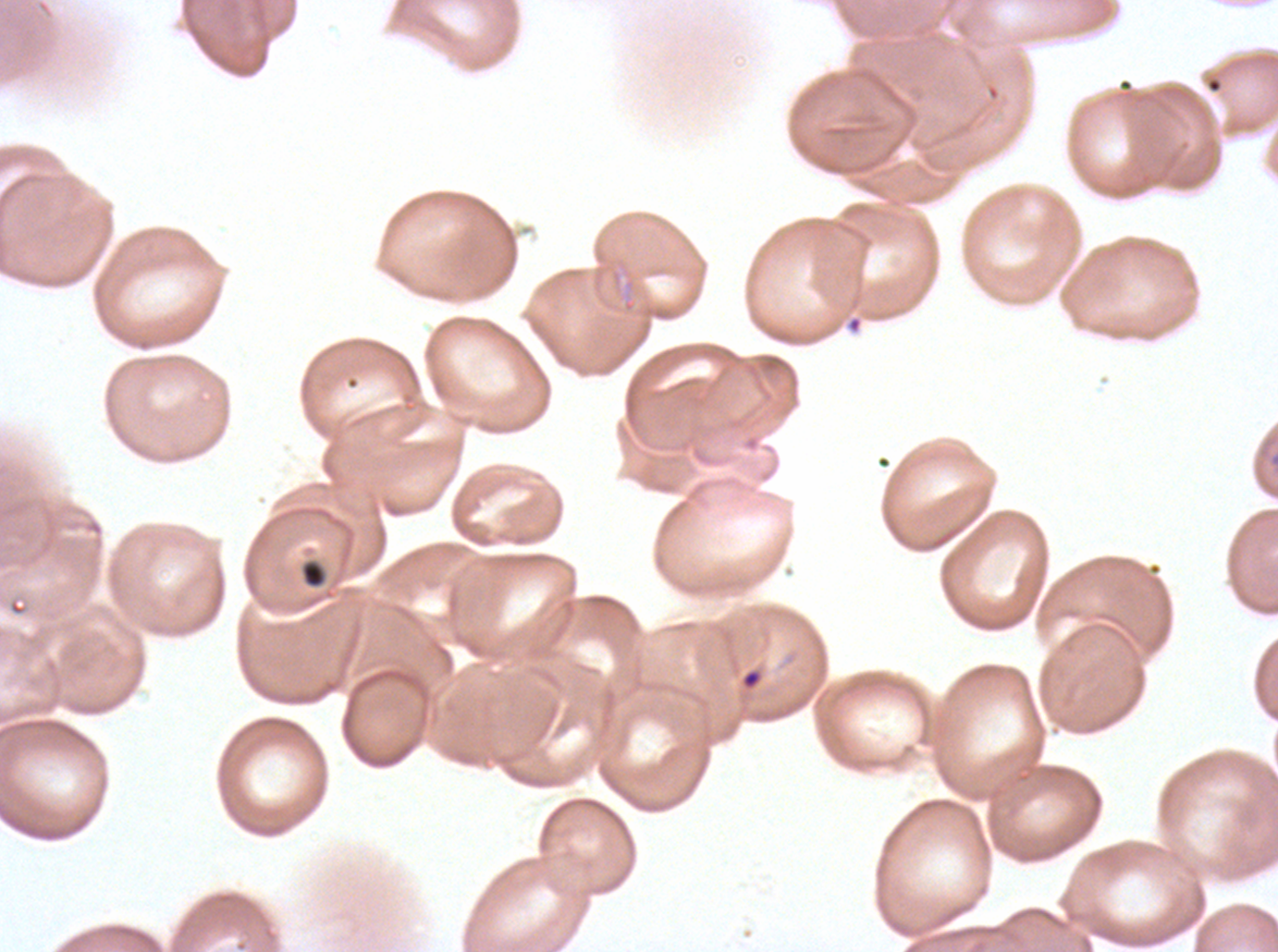

notation = approximate bounding rectangles given as corner coordinates in pixels from the top-left
ring locations = (x1=740, y1=667, x2=764, y2=691)
field of view = sub-image separated from a larger composite
image size = 1278×952 pixels
preparation = thin blood smear
stain = Giemsa
specimen = Plasmodium falciparum cultured ex vivo for 24 to 48 hours, from a patient in The Gambia